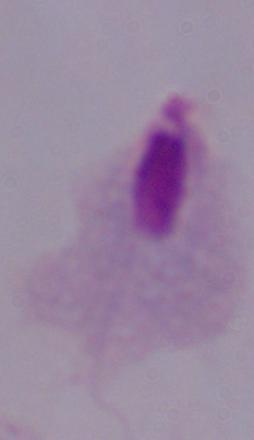 Captured at 1000x magnification. A trichomonad is seen. Micrograph.